Give the position of every leukocyte visible.
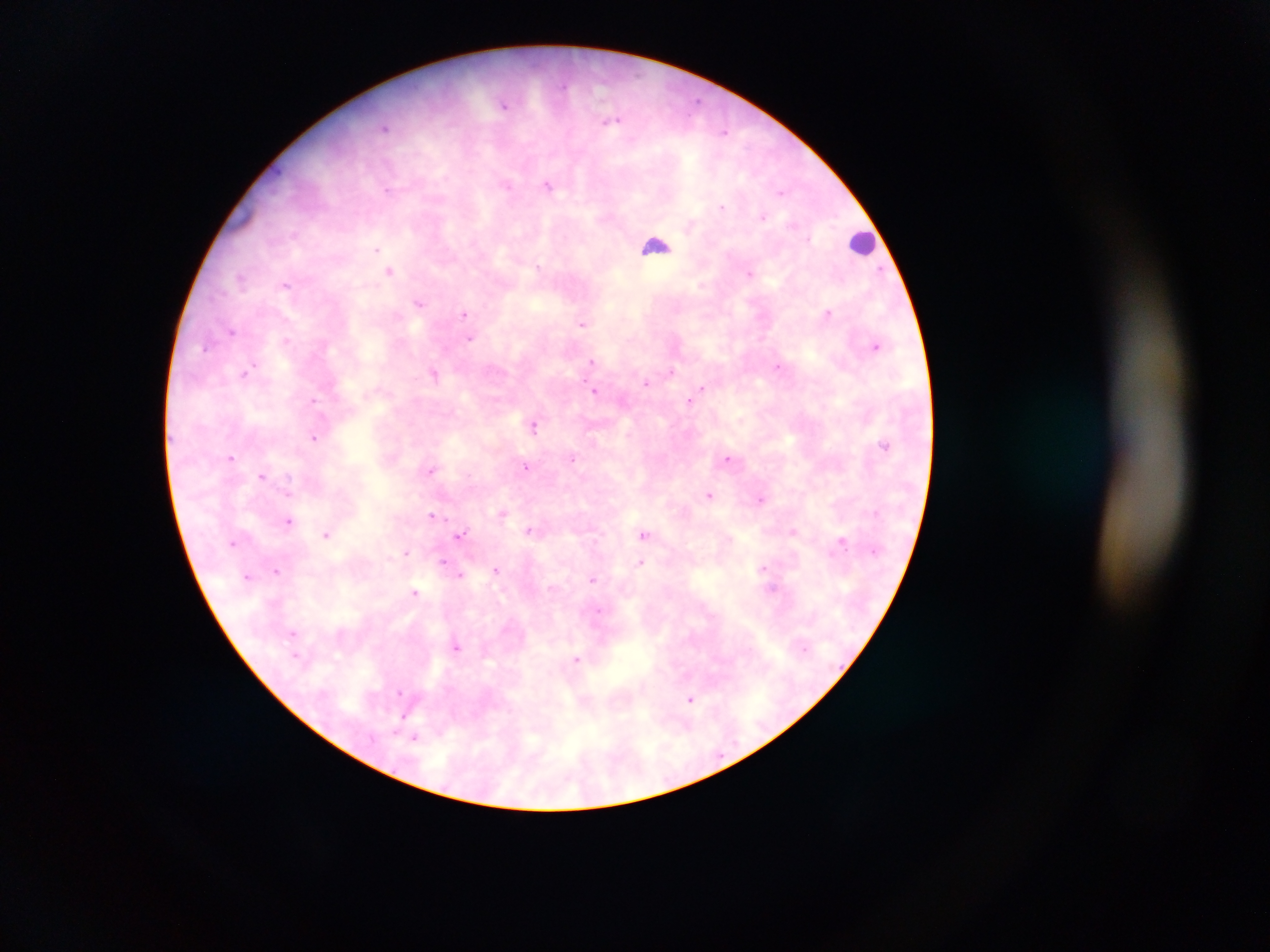

Approximate centers as (x, y) in pixels.
Leukocytes: (862, 242), (655, 245).

Summary:
  - Plasmodium parasite locations: (698, 101), (503, 105), (611, 121), (384, 127), (724, 132), (508, 186), (548, 186), (387, 189), (780, 192), (722, 207), (763, 217), (808, 238), (376, 249), (538, 267), (389, 271), (881, 271), (750, 273), (240, 278), (286, 285), (420, 303), (828, 313), (464, 314), (582, 323), (232, 331), (470, 339), (287, 340), (875, 346), (206, 347), (592, 361), (778, 367), (248, 370), (672, 371), (434, 374), (646, 382), (701, 388), (595, 391), (689, 400), (314, 401), (534, 425), (315, 438), (884, 444), (232, 457), (573, 458), (728, 458), (526, 466), (430, 470), (262, 476), (289, 493), (710, 495), (761, 499), (502, 514), (431, 515), (288, 521), (529, 530), (793, 531), (327, 534), (460, 534), (643, 534), (233, 542), (841, 542), (406, 553), (443, 561), (641, 562), (763, 568), (276, 570), (496, 570), (460, 575), (247, 576), (593, 579), (415, 592), (598, 612), (293, 633), (457, 647), (295, 654), (577, 660), (400, 692), (690, 699), (415, 737)
  - Image size: 1270×952 pixels
  - Capture: mobile-phone photograph through a microscope
  - Country: Ghana
  - Field of view: single
  - Preparation: thick blood smear